Identify the parasite.
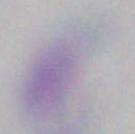
Toxoplasma gondii.

Photomicrograph. 1000x magnification.